Name the parasite shown.
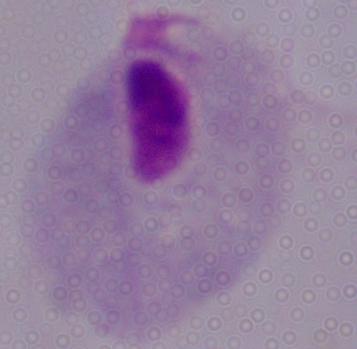
This is a trichomonad.

Photomicrograph. 1000x magnification.